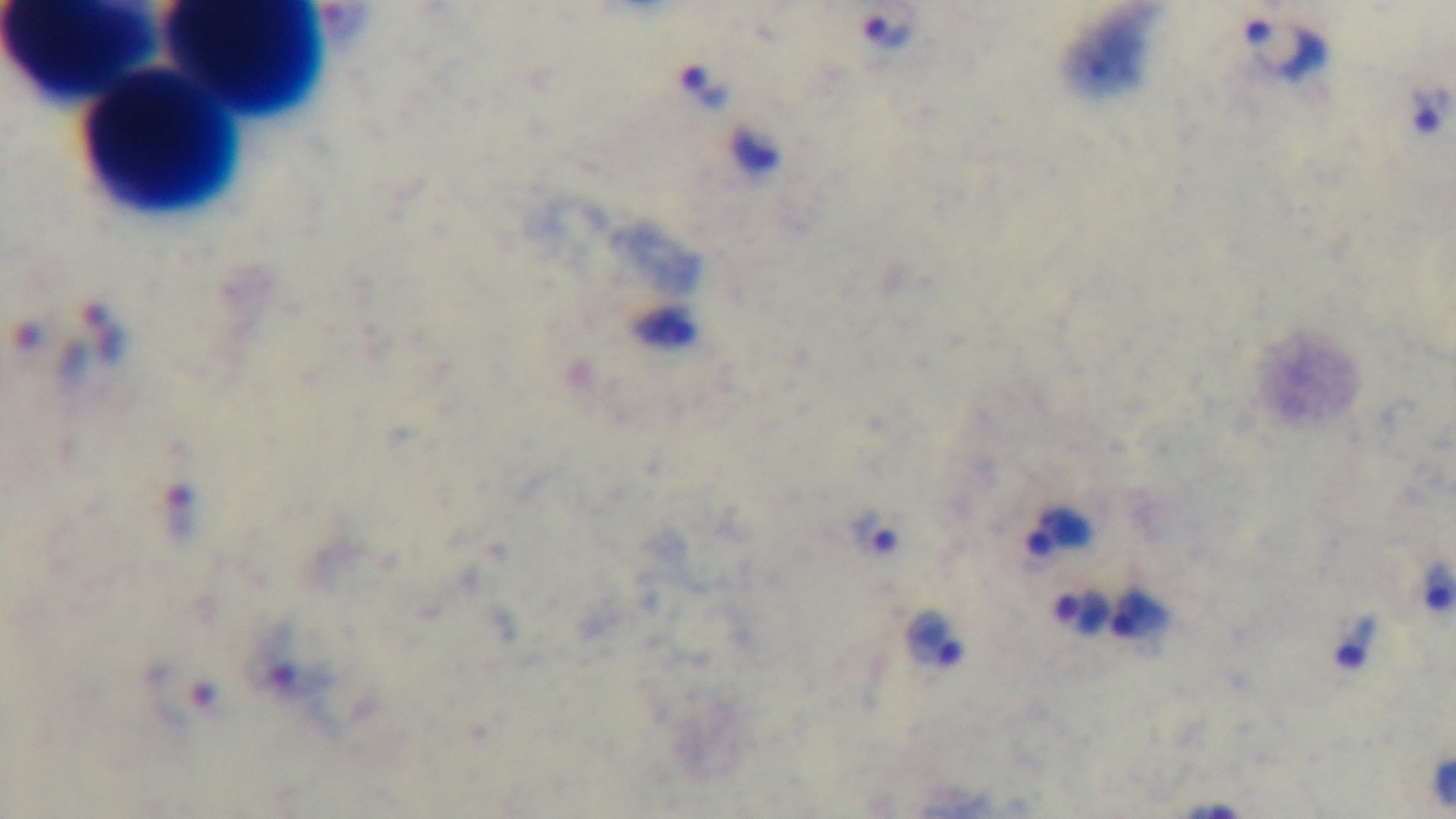

Summary:
  - Stain: Giemsa
  - Preparation: thick
  - Field of view: single
  - Modality: light microscopy
  - Objective: 100x oil immersion
  - Malaria status: positive
  - Capture: mounted 4K digital camera